Evaluate for Plasmodium parasites.
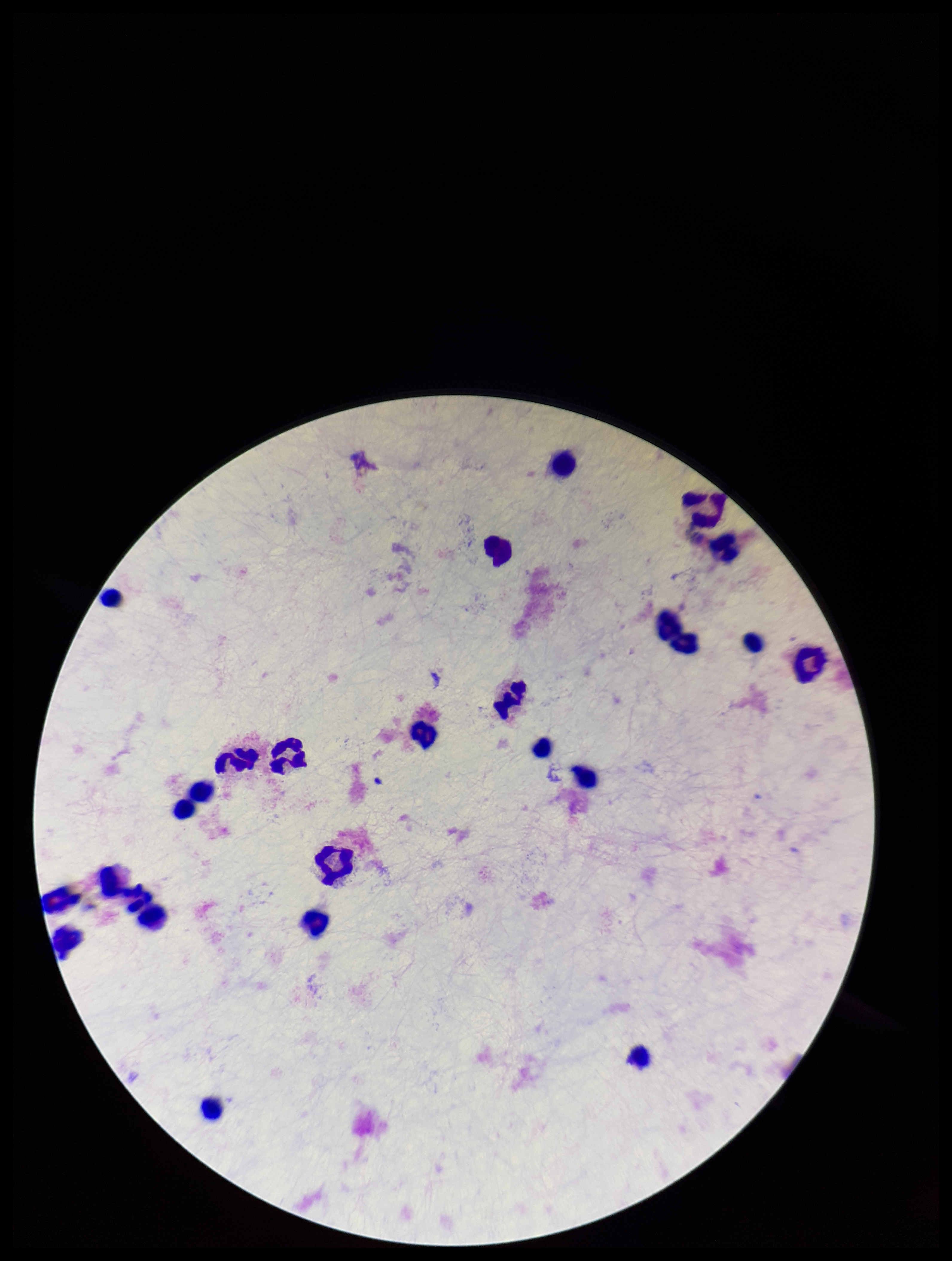

None detected.

Parasite count: 0. Giemsa stain. Leukocyte count: 23. Photographed through the microscope eyepiece with a smartphone camera. Patient malaria status: negative. Image is 952×1261 pixels. Preparation: thick. One field from this slide.